Locate every blood parasite and identify its species.
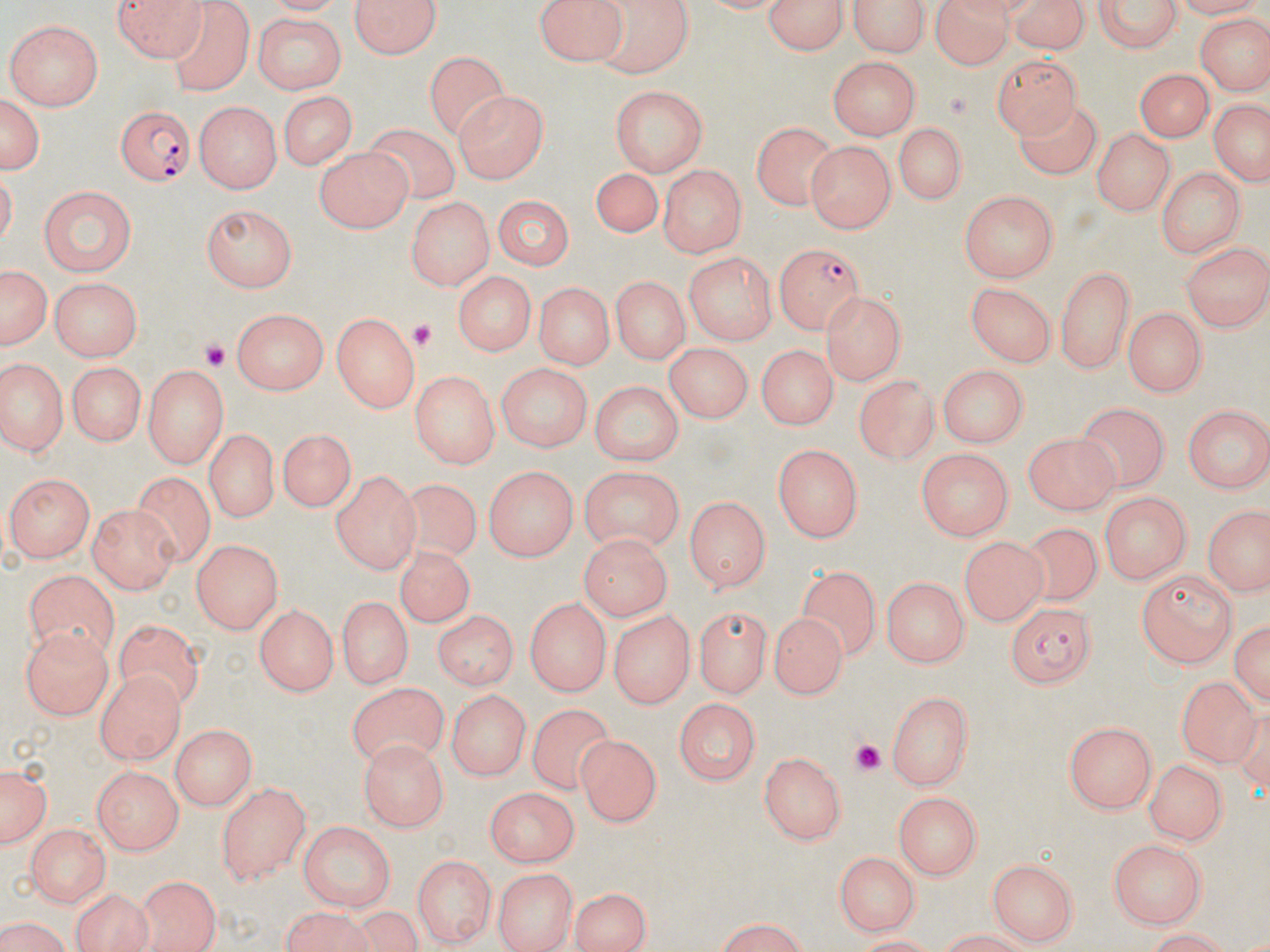

Approximate bounding boxes as (x1,y1)-(x2,y2) corner pairs in pixels.
Plasmodium falciparum-infected red blood cells: (113,102)-(197,183), (771,243)-(863,332), (1007,604)-(1097,687).
No Plasmodium ovale, Plasmodium malariae, Plasmodium vivax, Babesia divergens, or Trypanosoma brucei observed.

Summary:
  - Uninfected red blood cell locations: (107,0)-(209,59), (353,0)-(440,61), (537,0)-(624,65), (595,0)-(692,77), (767,0)-(845,59), (853,0)-(928,58), (929,0)-(1014,68), (1007,0)-(1093,54), (1090,0)-(1183,55), (162,3)-(251,97), (253,13)-(346,95), (1195,14)-(1267,95), (3,18)-(105,109), (423,48)-(509,135), (994,54)-(1082,132), (830,57)-(921,140), (1136,68)-(1214,141), (608,86)-(706,174), (2,91)-(44,176), (449,91)-(544,184), (275,93)-(358,171), (194,102)-(281,194), (1012,102)-(1103,181), (1205,102)-(1270,187), (752,119)-(838,209), (895,119)-(966,206), (364,124)-(462,202), (1093,129)-(1176,214), (805,139)-(895,233), (313,148)-(411,233), (655,164)-(746,256), (1155,165)-(1241,257), (591,167)-(665,234), (38,184)-(136,276), (960,190)-(1059,283), (488,193)-(574,274), (404,197)-(491,292), (201,203)-(299,291), (1182,240)-(1270,332), (684,253)-(777,344), (1058,263)-(1135,373), (1,266)-(48,353), (453,270)-(532,359), (612,276)-(686,364), (50,278)-(143,362), (530,282)-(615,373), (966,283)-(1053,367), (821,291)-(907,387), (230,308)-(328,394), (1120,308)-(1208,395), (332,314)-(422,413), (663,342)-(752,423), (756,342)-(837,427), (0,355)-(67,456), (66,361)-(145,448), (495,363)-(593,453), (940,363)-(1030,446), (141,365)-(227,465), (410,371)-(495,469), (855,373)-(938,465), (586,382)-(682,467), (1078,401)-(1170,492), (1185,405)-(1269,493), (279,424)-(358,509), (1023,429)-(1119,513), (202,430)-(279,522), (771,444)-(864,541), (916,449)-(1012,542), (482,462)-(577,561), (578,468)-(684,555), (330,471)-(421,574), (7,473)-(93,562), (136,473)-(217,568), (391,483)-(479,565), (1099,491)-(1193,585), (687,494)-(772,588), (89,505)-(179,592), (1205,506)-(1265,598), (1022,521)-(1103,603), (578,535)-(670,619), (960,535)-(1047,627), (191,541)-(282,635), (398,548)-(471,626), (798,564)-(880,659), (1136,567)-(1239,670), (23,569)-(121,654), (881,578)-(967,667), (334,594)-(408,692), (525,595)-(608,697), (692,607)-(773,697), (253,608)-(336,696), (435,609)-(516,691), (772,613)-(847,696), (612,614)-(693,704), (1233,617)-(1269,705), (116,622)-(203,712), (19,628)-(113,720), (1175,671)-(1261,765), (94,673)-(182,764), (347,683)-(448,767), (884,689)-(975,790), (449,690)-(527,782), (670,699)-(761,782), (529,706)-(614,796), (1063,722)-(1158,813), (168,725)-(252,810), (571,732)-(660,826), (359,740)-(446,831), (759,752)-(848,846), (1144,760)-(1221,844), (2,762)-(50,851), (89,768)-(181,855), (217,784)-(309,883), (482,785)-(580,865), (895,794)-(983,879), (298,821)-(395,910), (22,822)-(112,905), (1108,837)-(1207,928), (836,848)-(920,935), (412,853)-(494,947), (988,858)-(1080,943), (492,866)-(578,952), (137,880)-(219,952), (565,888)-(652,952), (71,890)-(153,952), (282,907)-(376,952), (0,919)-(77,952), (706,922)-(821,951), (914,925)-(1039,951), (1134,928)-(1238,951)
  - Platelet locations: (409,319)-(436,350), (197,338)-(230,371), (851,739)-(885,777)
  - Slide-level diagnosis: Plasmodium falciparum
  - Image size: 1270×952 pixels
  - Stain: May-Grünwald-Giemsa
  - Modality: optical microscopy
  - Field of view: single
  - Preparation: thin blood film
  - Magnification: 1000x